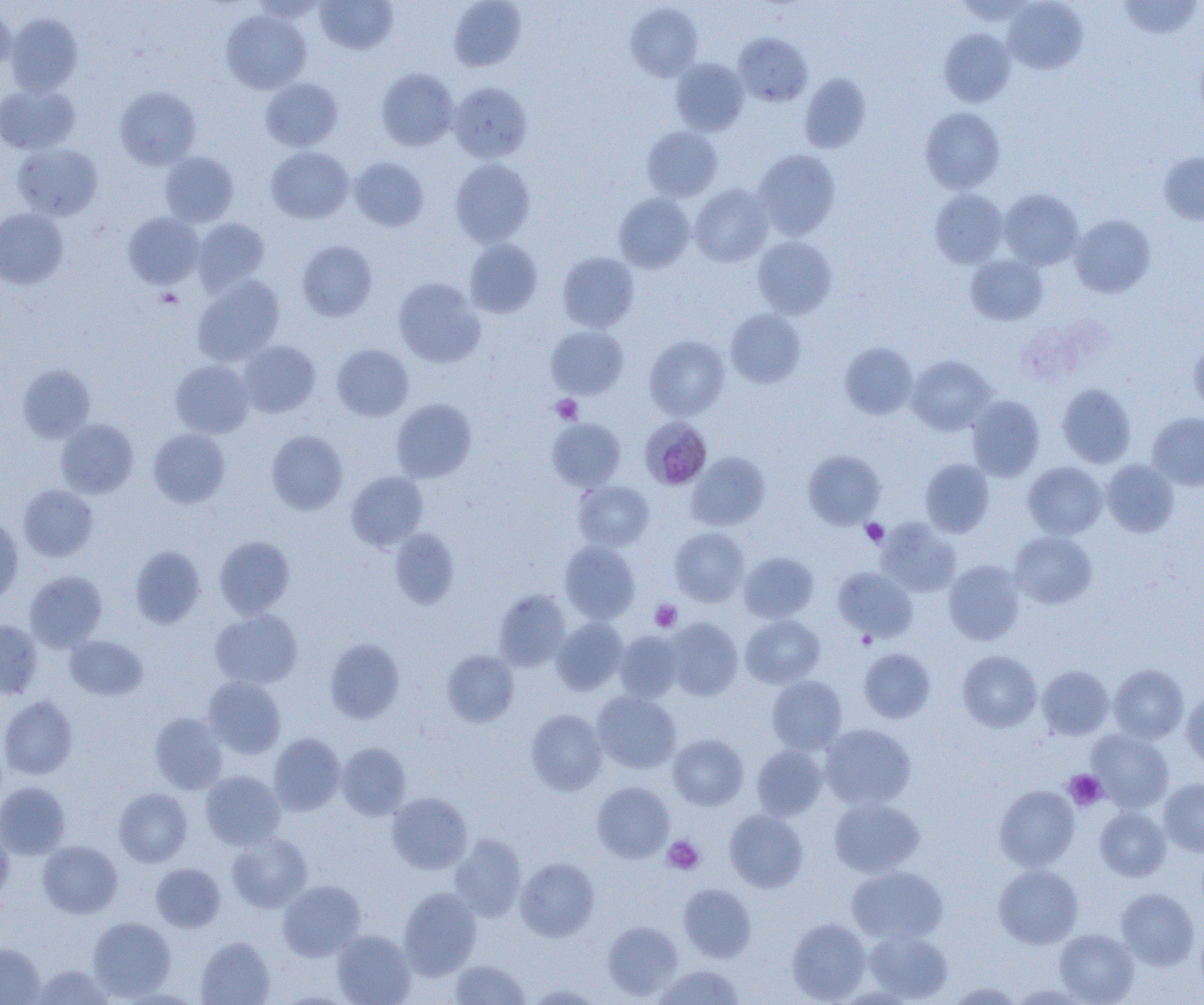
Approximate bounding boxes as [x1, y1, x2, y2] in pixels. Platelet locations: [156, 288, 183, 308], [551, 394, 583, 424], [860, 518, 889, 547], [649, 599, 681, 632], [857, 631, 877, 650], [1063, 769, 1107, 810], [663, 836, 704, 874]. Plasmodium malariae-infected red blood cell locations: [639, 415, 712, 490]. Uninfected red blood cell locations: [315, 0, 398, 54], [448, 0, 525, 72], [1003, 0, 1088, 73], [1118, 0, 1202, 40], [626, 3, 703, 82], [0, 5, 15, 72], [221, 10, 311, 94], [6, 13, 83, 96], [939, 29, 1016, 107], [734, 32, 813, 107], [670, 58, 749, 136], [376, 68, 459, 151], [799, 73, 871, 153], [260, 78, 343, 151], [448, 82, 532, 163], [0, 83, 80, 154], [115, 87, 201, 169], [920, 107, 1005, 194], [642, 126, 722, 201], [13, 143, 103, 220], [266, 146, 354, 223], [754, 149, 840, 240], [159, 151, 239, 227], [1158, 152, 1204, 225], [349, 157, 429, 231], [450, 158, 535, 247], [690, 183, 773, 267], [999, 189, 1084, 270], [930, 190, 1007, 268], [613, 193, 695, 272], [0, 208, 68, 289], [123, 212, 203, 289], [1071, 214, 1156, 298], [192, 218, 269, 294], [753, 236, 837, 318], [465, 239, 542, 318], [297, 240, 377, 321], [558, 252, 639, 333], [966, 255, 1047, 325], [192, 275, 284, 366], [393, 277, 485, 367], [726, 309, 806, 387], [546, 325, 628, 398], [644, 335, 730, 420], [1189, 338, 1204, 416], [238, 340, 320, 417], [840, 343, 918, 419], [332, 344, 413, 421], [907, 355, 996, 435], [170, 360, 254, 438], [18, 364, 95, 442], [1057, 383, 1136, 468], [967, 395, 1044, 481], [392, 399, 476, 482], [1147, 412, 1204, 491], [546, 418, 626, 491], [55, 419, 138, 498], [148, 428, 230, 508], [266, 430, 348, 514], [803, 450, 885, 528], [687, 452, 770, 530], [920, 459, 994, 537], [1101, 459, 1179, 537], [1023, 462, 1107, 539], [346, 471, 427, 551], [573, 480, 654, 551], [18, 484, 97, 562], [0, 517, 23, 604], [876, 518, 960, 597], [669, 527, 749, 606], [389, 528, 459, 609], [1009, 531, 1097, 609], [214, 536, 295, 619], [560, 541, 639, 623], [130, 546, 205, 628], [738, 552, 818, 623], [944, 560, 1025, 645], [832, 567, 918, 642], [25, 570, 106, 652], [494, 589, 571, 670], [210, 609, 302, 689], [741, 614, 824, 689], [551, 618, 628, 695], [666, 618, 742, 700], [0, 619, 42, 700], [614, 631, 683, 703], [65, 635, 147, 701], [325, 638, 404, 723], [859, 648, 935, 724], [442, 650, 519, 727], [958, 650, 1042, 732], [1108, 664, 1188, 744], [1037, 665, 1114, 740], [203, 676, 286, 759], [767, 676, 847, 754], [1181, 689, 1204, 771], [592, 691, 681, 773], [0, 696, 78, 780], [526, 709, 607, 795], [150, 712, 228, 794], [821, 723, 916, 809], [1087, 729, 1174, 813], [269, 733, 345, 815], [668, 734, 748, 810], [337, 743, 411, 819], [751, 745, 827, 820], [200, 770, 285, 850], [1158, 778, 1204, 857], [592, 781, 674, 862], [0, 782, 70, 859], [995, 785, 1079, 870], [114, 788, 192, 866], [387, 792, 472, 873], [829, 797, 924, 877], [1095, 807, 1171, 881], [724, 809, 809, 892], [0, 826, 13, 906], [228, 833, 312, 912], [449, 834, 526, 921], [38, 841, 122, 918], [515, 857, 599, 941], [151, 863, 225, 931], [994, 863, 1084, 949], [847, 865, 948, 945], [278, 880, 365, 961], [679, 883, 756, 963], [399, 887, 481, 978], [1116, 887, 1200, 971], [87, 917, 175, 1000], [787, 918, 871, 1003], [602, 920, 682, 1000], [332, 929, 415, 1005], [862, 929, 952, 1002], [1055, 929, 1139, 1004], [196, 936, 274, 1005], [0, 943, 45, 1004], [450, 959, 530, 1004], [31, 963, 114, 1004], [652, 965, 746, 1005], [945, 981, 1024, 1004], [526, 983, 604, 1004], [1009, 983, 1090, 1004]. Slide-level diagnosis: Plasmodium malariae. Single field of view. Image is 1204×1005 pixels. Light microscopy. Captured at 1000x magnification. Thin blood film.